Identify the preparation type.
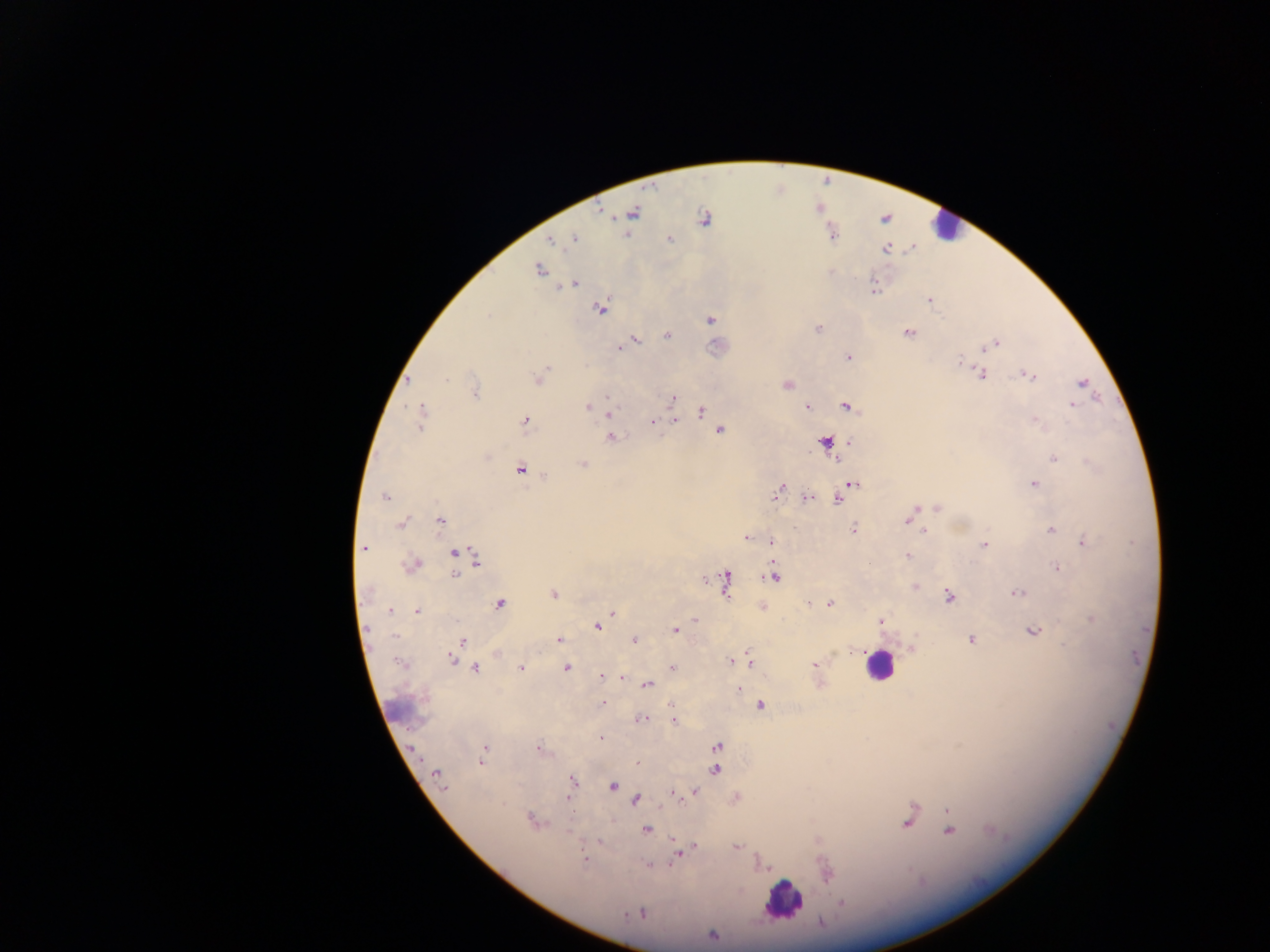

Thick blood smear.

Approximate centers as [x, y] in pixels.
Summary:
  - Malaria parasite locations: [634, 212], [703, 218], [627, 233], [573, 239], [671, 241], [550, 242], [538, 271], [575, 282], [570, 285], [875, 290], [929, 300], [601, 309], [488, 316], [709, 319], [819, 328], [909, 331], [667, 336], [638, 339], [996, 342], [620, 346], [992, 347], [847, 358], [956, 359], [546, 369], [982, 374], [1033, 375], [540, 376], [447, 380], [1082, 382], [788, 386], [477, 390], [606, 395], [672, 398], [807, 406], [1072, 406], [587, 408], [846, 408], [702, 410], [422, 411], [602, 413], [609, 414], [524, 420], [1036, 420], [676, 421], [653, 423], [720, 431], [610, 438], [848, 441], [1052, 457], [834, 458], [1085, 461], [582, 464], [544, 475], [1034, 483], [856, 484], [779, 489], [807, 495], [775, 496], [386, 497], [837, 500], [935, 508], [440, 520], [399, 522], [917, 527], [853, 528], [1051, 529], [923, 531], [746, 537], [1083, 541], [773, 542], [983, 545], [364, 549], [454, 553], [908, 555], [476, 561], [416, 564], [1056, 566], [773, 572], [456, 575], [725, 578], [774, 578], [914, 585], [727, 586], [1015, 593], [364, 594], [553, 595], [947, 595], [830, 603], [417, 611], [389, 612], [397, 613], [611, 613], [1089, 618], [695, 620], [880, 621], [597, 628], [368, 629], [674, 629], [1034, 630], [395, 635], [972, 639], [634, 640], [464, 641], [560, 641], [746, 652], [834, 653], [452, 660], [729, 660], [399, 662], [734, 662], [751, 663], [815, 665], [672, 666], [477, 668], [520, 669], [567, 669], [600, 678], [623, 679], [820, 684], [648, 685], [739, 689], [602, 703], [671, 703], [761, 705], [642, 718], [673, 722], [599, 739], [718, 746], [958, 746], [485, 747], [537, 748], [415, 749], [481, 763], [637, 764], [717, 770], [435, 773], [572, 780], [612, 787], [696, 791], [569, 792], [673, 793], [567, 799], [637, 800], [947, 810], [528, 818], [907, 822], [546, 823], [569, 830], [645, 830], [949, 832], [673, 839], [599, 842], [696, 846], [737, 847], [676, 857], [584, 859], [647, 866], [920, 883], [842, 903], [641, 913], [711, 934]
  - Leukocyte locations: [937, 231], [878, 667], [780, 898]
  - Country: Ghana
  - Field of view: single
  - Capture: mobile-phone photograph through a microscope
  - Image size: 1270×952 pixels